Outline each blood parasite and name the species.
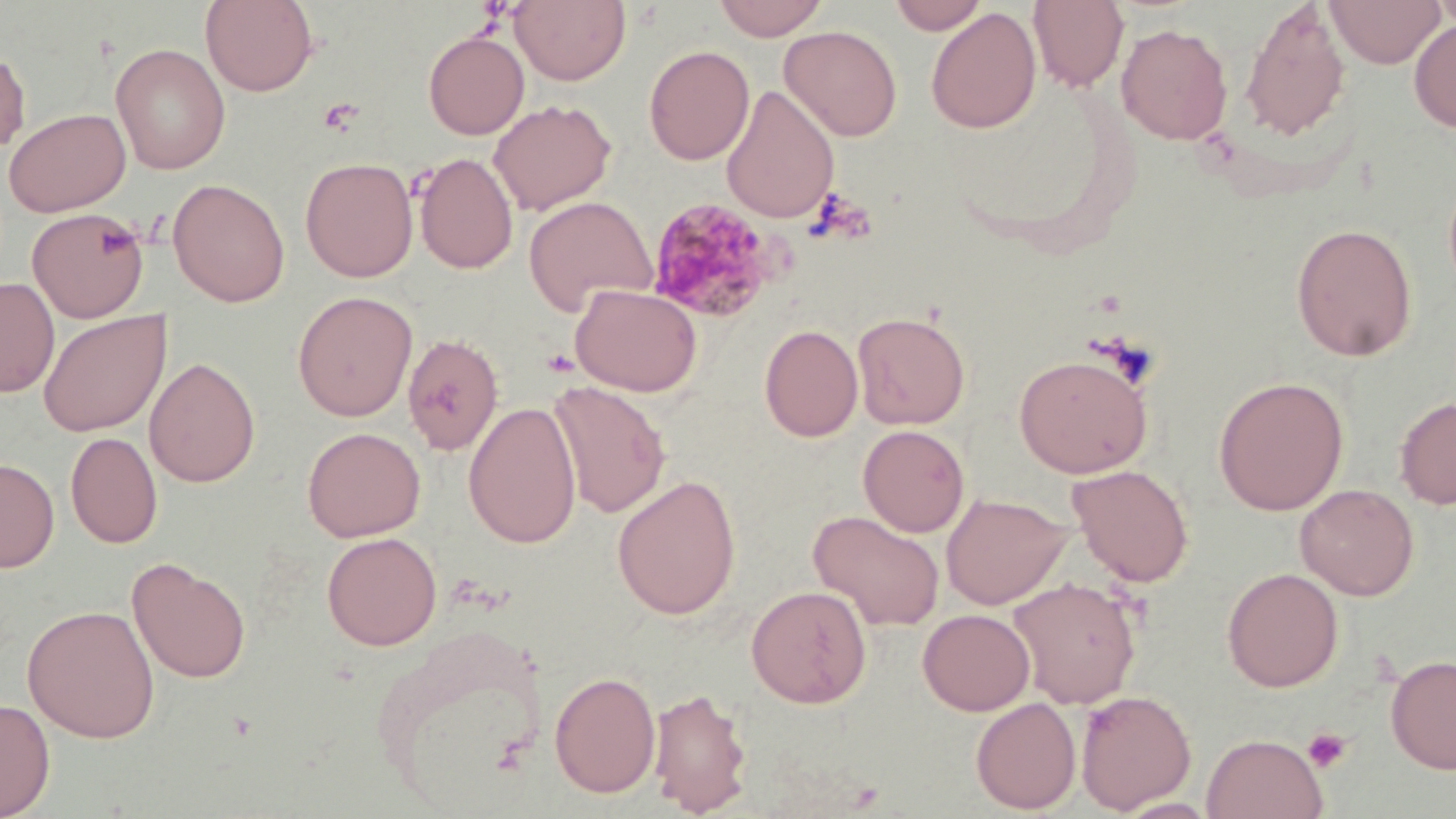

Approximate bounding boxes as (x1,y1)-(x2,y2) corner pairs in pixels.
Plasmodium malariae-infected red blood cells: (646,196)-(781,323).
No Plasmodium falciparum, Plasmodium ovale, Plasmodium vivax, Babesia divergens, or Trypanosoma brucei observed.

slide-level diagnosis = Plasmodium malariae
field of view = single
image size = 1456×819 pixels
preparation = thin blood smear
stain = May-Grünwald-Giemsa
platelet locations = approximate bounding boxes as (x1,y1)-(x2,y2) corner pairs in pixels: (319,96)-(365,136), (805,187)-(876,245), (1303,727)-(1352,773)
uninfected red blood cell locations = approximate bounding boxes as (x1,y1)-(x2,y2) corner pairs in pixels: (200,0)-(319,96), (712,0)-(829,41), (889,0)-(989,34), (1028,0)-(1129,91), (1324,0)-(1447,68), (1432,0)-(1456,38), (510,1)-(631,86), (1240,3)-(1351,142), (925,7)-(1041,134), (1409,18)-(1456,134), (1115,23)-(1233,145), (779,25)-(902,141), (423,30)-(529,140), (110,43)-(231,175), (643,44)-(755,165), (0,47)-(31,157), (721,85)-(840,224), (488,99)-(617,215), (3,107)-(131,218), (414,152)-(518,275), (300,157)-(418,282), (168,178)-(290,307), (524,195)-(657,314), (27,208)-(149,323), (1290,223)-(1418,362), (0,278)-(59,397), (570,284)-(702,397), (292,291)-(417,421), (39,310)-(170,438), (852,311)-(971,430), (759,323)-(863,442), (402,332)-(504,455), (1013,352)-(1153,478), (144,356)-(261,488), (1213,375)-(1349,515), (548,381)-(671,518), (1395,395)-(1456,510), (463,401)-(582,549), (857,424)-(969,537), (302,426)-(425,542), (65,431)-(163,549), (0,458)-(59,572), (1067,463)-(1194,587), (611,474)-(742,620), (1295,483)-(1419,601), (940,492)-(1071,610), (808,509)-(945,632), (321,531)-(442,650), (127,557)-(251,684), (1222,567)-(1344,692), (1008,577)-(1142,708), (746,585)-(872,708), (22,604)-(160,743), (918,609)-(1035,715), (363,623)-(554,805), (1385,653)-(1456,774), (549,670)-(661,798), (648,685)-(752,815), (1076,689)-(1196,812), (970,696)-(1081,814), (0,697)-(55,819), (1201,733)-(1327,818)
magnification = 1000x
modality = optical microscopy